Point out each malaria parasite and each leukocyte.
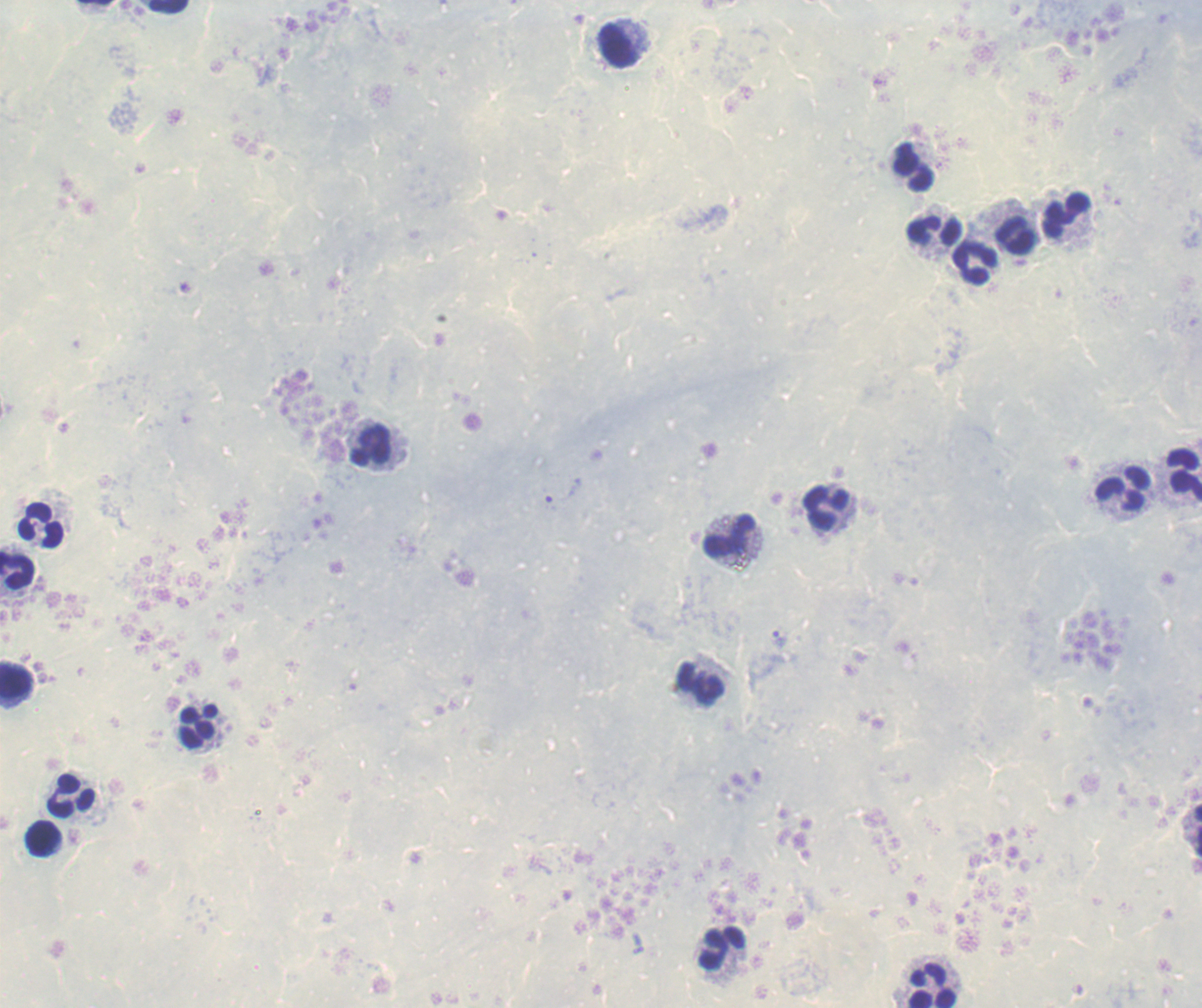

Approximate centers as {x, y} in pixels.
Trophozoites: {563, 492}, {781, 640}.
No schizont or gametocyte forms observed.
Leukocytes: {169, 7}, {618, 44}, {914, 169}, {1066, 213}, {934, 231}, {1016, 236}, {975, 263}, {371, 445}, {1184, 476}, {1122, 488}, {826, 508}, {41, 526}, {729, 535}, {17, 570}, {17, 679}, {700, 683}, {198, 726}, {72, 795}, {43, 838}, {721, 949}, {931, 985}.

Summary:
  - Context: previously used in a real diagnosis
  - Image size: 1202×1008 pixels
  - Preparation: thick smear of blood
  - Field of view: one from this slide
  - Stain: Romanowsky
  - Magnification: 100x
  - Background quality: unsatisfactory